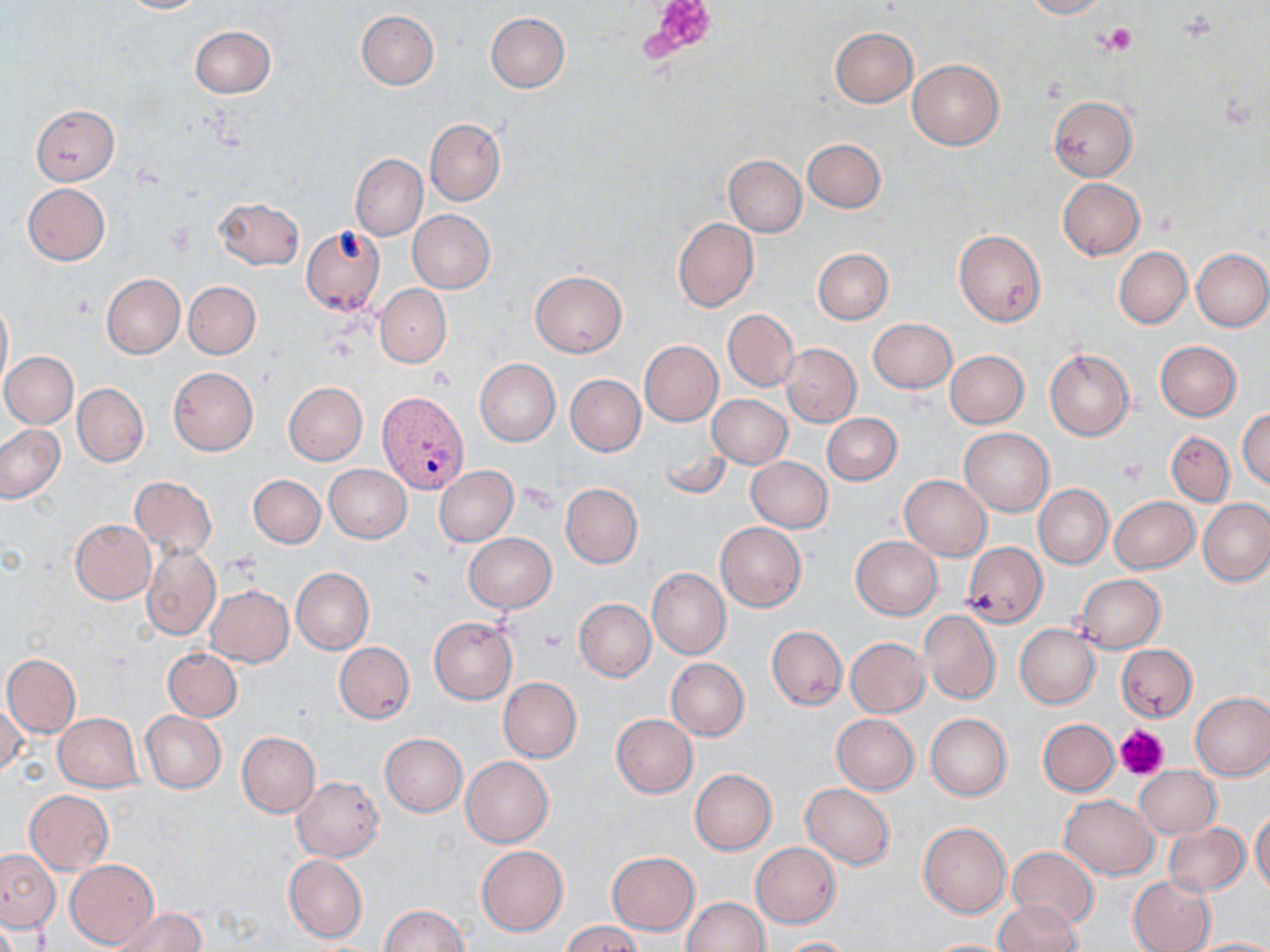
Summary:
  - Coordinate format: approximate bounding boxes as [x1, y1, x2, y2] in pixels
  - Plasmodium vivax-infected red blood cell locations: [379, 388, 472, 492]
  - Uninfected red blood cell locations: [119, 0, 205, 14], [1024, 0, 1109, 19], [357, 11, 439, 90], [486, 13, 570, 92], [190, 25, 275, 98], [830, 27, 917, 107], [908, 59, 1003, 150], [1048, 97, 1136, 182], [31, 104, 120, 185], [424, 118, 504, 207], [802, 139, 886, 213], [350, 153, 427, 239], [723, 154, 806, 237], [1057, 178, 1144, 259], [23, 183, 110, 265], [214, 197, 304, 270], [407, 209, 495, 292], [673, 217, 759, 312], [300, 225, 386, 315], [954, 231, 1046, 327], [1114, 247, 1191, 328], [1191, 248, 1270, 331], [813, 249, 893, 324], [530, 270, 627, 357], [102, 274, 185, 358], [184, 281, 261, 359], [375, 284, 451, 368], [0, 297, 12, 396], [723, 308, 799, 393], [867, 318, 957, 393], [640, 340, 722, 427], [1155, 340, 1242, 420], [781, 343, 861, 426], [1045, 349, 1133, 441], [1, 351, 78, 429], [945, 351, 1029, 429], [475, 359, 560, 445], [167, 367, 258, 456], [565, 374, 645, 457], [283, 381, 367, 465], [73, 383, 148, 466], [707, 394, 792, 468], [1237, 407, 1270, 490], [821, 413, 901, 485], [0, 423, 65, 503], [960, 428, 1054, 515], [1167, 432, 1235, 506], [657, 444, 732, 500], [746, 456, 833, 532], [325, 464, 411, 543], [434, 465, 519, 547], [249, 475, 326, 549], [899, 475, 992, 560], [130, 476, 217, 559], [560, 483, 642, 567], [1034, 484, 1113, 568], [1109, 496, 1198, 573], [1198, 499, 1270, 587], [71, 519, 156, 604], [715, 522, 807, 612], [464, 533, 555, 613], [850, 536, 942, 619], [962, 542, 1048, 626], [142, 543, 221, 640], [647, 567, 731, 659], [292, 568, 373, 654], [1076, 574, 1165, 652], [206, 585, 294, 667], [574, 599, 655, 682], [919, 610, 1000, 703], [429, 617, 517, 703], [1015, 624, 1099, 708], [767, 625, 847, 709], [845, 638, 929, 718], [334, 642, 415, 724], [1116, 643, 1197, 722], [164, 648, 242, 722], [3, 655, 81, 737], [666, 658, 749, 741], [498, 677, 582, 762], [1190, 690, 1270, 780], [1, 699, 26, 778], [141, 711, 226, 793], [54, 713, 145, 792], [612, 714, 697, 797], [832, 714, 919, 794], [925, 714, 1012, 801], [1038, 719, 1119, 796], [236, 731, 320, 816], [380, 733, 467, 816], [462, 757, 553, 847], [1134, 766, 1221, 839], [690, 770, 776, 855], [292, 776, 383, 862], [801, 784, 895, 869], [25, 790, 114, 873], [1060, 795, 1157, 878], [1250, 808, 1270, 897], [918, 821, 1012, 918], [1163, 823, 1250, 897], [751, 842, 841, 927], [477, 845, 567, 935], [1007, 847, 1100, 929], [1, 849, 60, 932], [607, 851, 700, 934], [283, 854, 367, 943], [66, 859, 158, 948], [1128, 875, 1215, 952], [682, 896, 768, 951], [994, 900, 1082, 952], [378, 905, 468, 952], [108, 907, 207, 952], [562, 921, 643, 952], [777, 937, 861, 952], [1186, 937, 1270, 952], [920, 939, 1017, 952]
  - Platelet locations: [645, 0, 720, 63], [1101, 23, 1137, 55], [428, 368, 455, 391], [1116, 457, 1147, 487], [540, 627, 570, 652], [1115, 724, 1170, 782]
  - Slide-level diagnosis: Plasmodium vivax
  - Modality: light microscopy
  - Field of view: one of a larger specimen
  - Preparation: thin blood smear
  - Magnification: 1000x
  - Stain: May-Grünwald-Giemsa
  - Image size: 1270×952 pixels